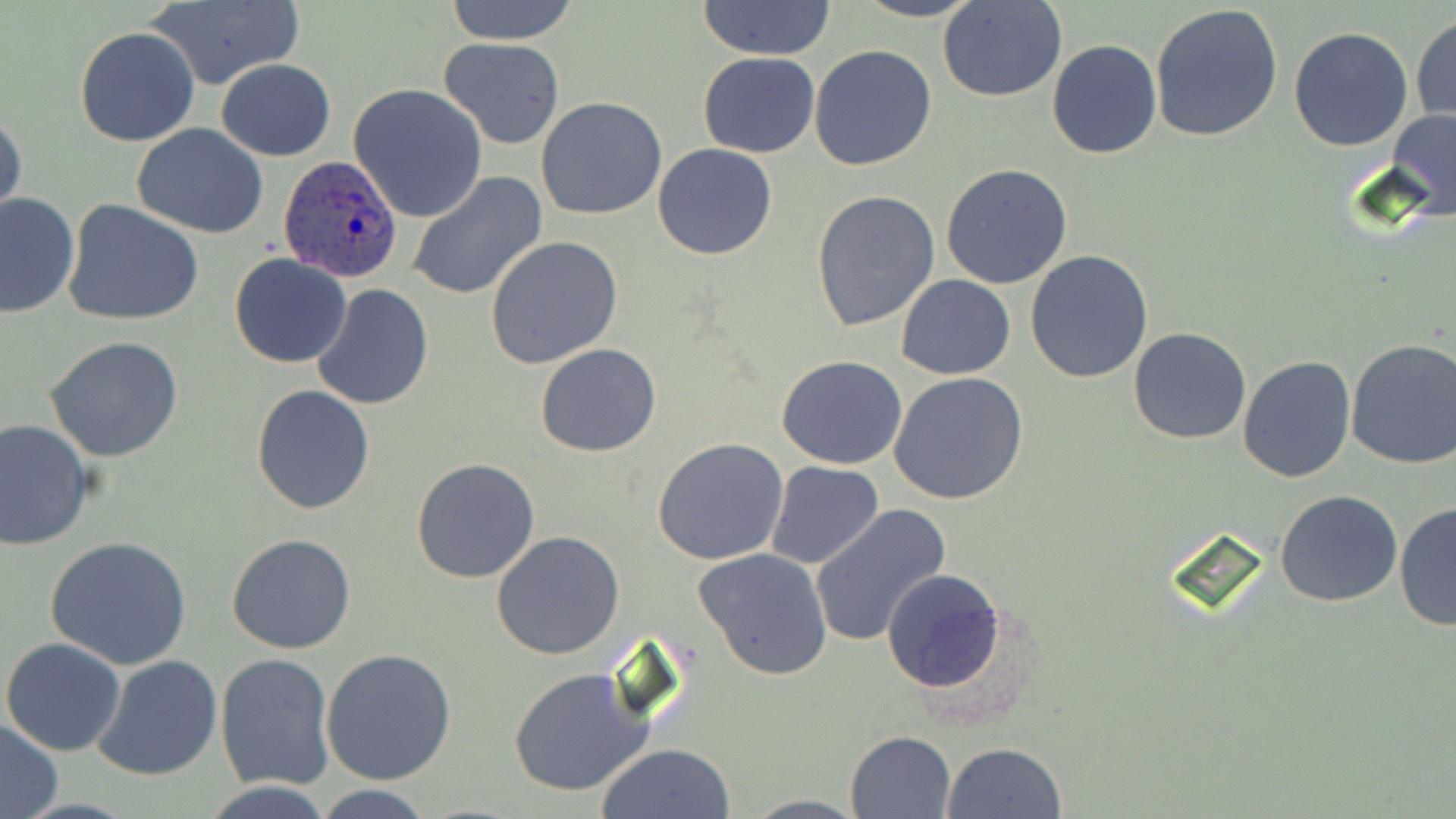

Summary:
  - Coordinate format: approximate bounding boxes as [x1, y1, x2, y2] in pixels
  - Plasmodium ovale-infected red blood cell locations: [279, 154, 403, 283]
  - Uninfected red blood cell locations: [444, 0, 580, 44], [852, 0, 984, 22], [143, 1, 304, 91], [695, 1, 837, 58], [939, 1, 1068, 102], [1149, 3, 1284, 143], [1410, 14, 1455, 124], [75, 26, 200, 147], [1288, 26, 1415, 152], [439, 36, 566, 148], [1047, 39, 1162, 158], [809, 44, 938, 172], [697, 51, 820, 158], [216, 59, 336, 161], [348, 83, 488, 222], [536, 96, 666, 220], [0, 107, 26, 227], [1387, 109, 1456, 221], [133, 124, 269, 238], [652, 143, 778, 260], [940, 163, 1072, 289], [406, 172, 548, 301], [810, 190, 941, 332], [1, 192, 80, 319], [63, 199, 204, 328], [485, 236, 624, 370], [1024, 249, 1154, 382], [228, 254, 353, 369], [896, 274, 1015, 380], [312, 284, 434, 411], [1128, 328, 1252, 445], [45, 335, 185, 462], [1344, 338, 1456, 470], [535, 344, 661, 458], [777, 355, 908, 470], [1237, 355, 1358, 483], [889, 372, 1029, 506], [252, 384, 375, 514], [0, 418, 94, 550], [652, 439, 790, 566], [411, 458, 540, 583], [766, 460, 884, 569], [1275, 489, 1402, 606], [1395, 501, 1455, 634], [809, 504, 949, 648], [491, 532, 625, 661], [226, 533, 357, 654], [46, 535, 193, 669], [694, 549, 833, 681], [882, 568, 1006, 694], [2, 637, 126, 756], [321, 647, 456, 785], [215, 652, 336, 791], [91, 654, 224, 779], [508, 667, 655, 798], [0, 719, 64, 818], [845, 731, 956, 818], [596, 743, 735, 819], [942, 743, 1067, 819], [201, 781, 336, 818], [313, 786, 435, 818], [739, 794, 867, 818]
  - Slide-level diagnosis: Plasmodium ovale
  - Modality: light microscopy
  - Stain: May-Grünwald-Giemsa
  - Preparation: thin blood smear
  - Field of view: single
  - Magnification: 1000x
  - Image size: 1456×819 pixels